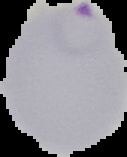
{
  "image_type": "segmented cell region with the area outside set to black",
  "image_size": "127×157 pixels",
  "preparation": "thin blood film",
  "malaria_status": "parasitized"
}